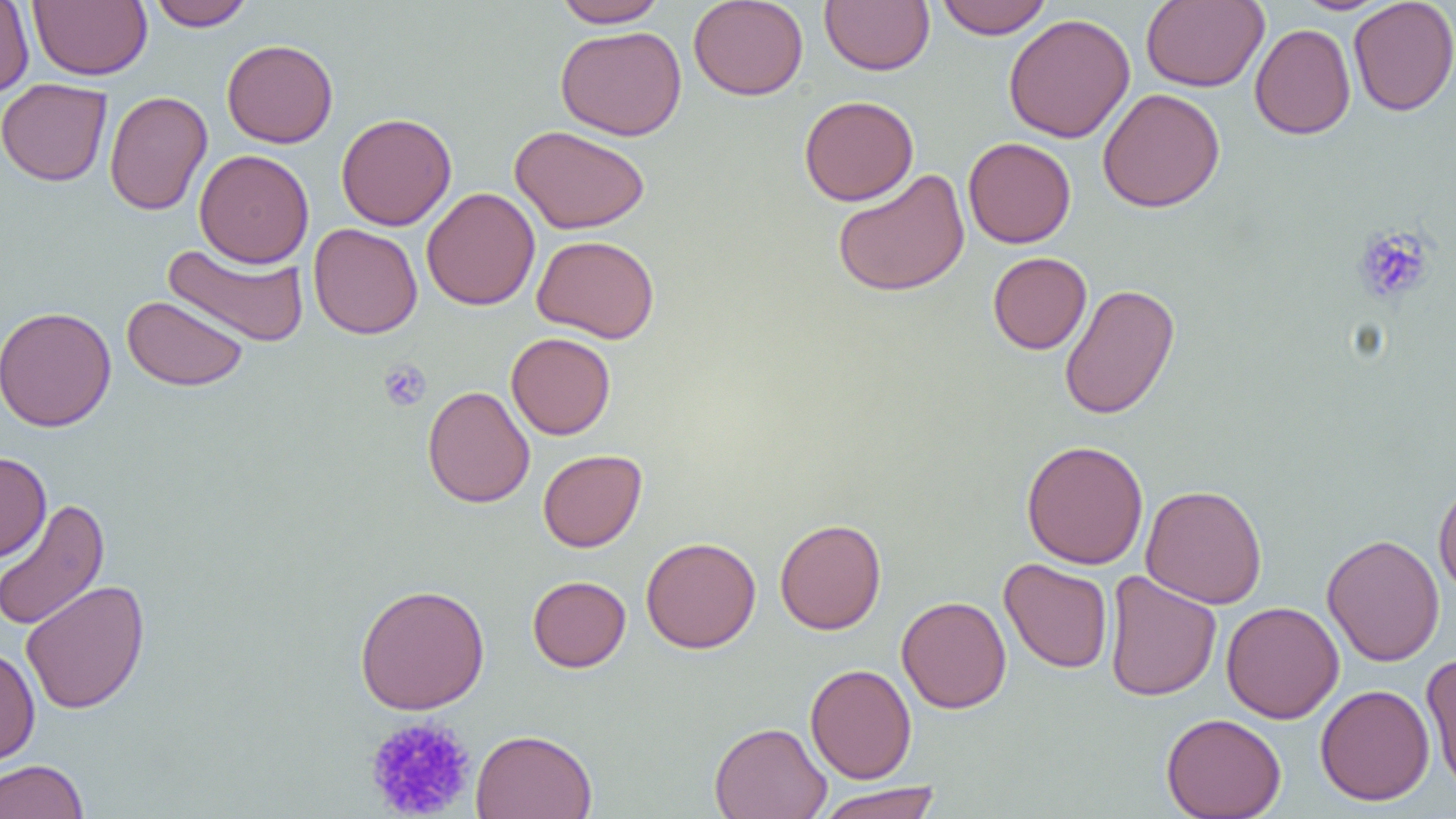
slide-level diagnosis = no evidence of blood parasites
modality = optical microscopy
uninfected red blood cell locations = approximate bounding boxes as named x1/y1/x2/y2 corners in pixels: (x1=0, y1=0, x2=35, y2=99), (x1=28, y1=0, x2=152, y2=81), (x1=146, y1=0, x2=255, y2=31), (x1=551, y1=0, x2=670, y2=28), (x1=688, y1=0, x2=809, y2=101), (x1=819, y1=0, x2=935, y2=75), (x1=935, y1=0, x2=1053, y2=39), (x1=1141, y1=0, x2=1269, y2=91), (x1=1290, y1=0, x2=1396, y2=15), (x1=1348, y1=0, x2=1456, y2=116), (x1=1003, y1=13, x2=1135, y2=143), (x1=1250, y1=23, x2=1356, y2=139), (x1=555, y1=25, x2=686, y2=140), (x1=222, y1=39, x2=339, y2=148), (x1=0, y1=78, x2=112, y2=186), (x1=1097, y1=88, x2=1225, y2=213), (x1=104, y1=90, x2=212, y2=216), (x1=798, y1=95, x2=918, y2=206), (x1=336, y1=112, x2=457, y2=231), (x1=510, y1=124, x2=650, y2=234), (x1=963, y1=137, x2=1076, y2=248), (x1=195, y1=149, x2=314, y2=268), (x1=832, y1=168, x2=970, y2=297), (x1=422, y1=187, x2=540, y2=311), (x1=308, y1=223, x2=423, y2=339), (x1=532, y1=235, x2=660, y2=343), (x1=163, y1=242, x2=309, y2=348), (x1=987, y1=252, x2=1092, y2=355), (x1=1059, y1=283, x2=1180, y2=420), (x1=121, y1=295, x2=249, y2=391), (x1=0, y1=305, x2=116, y2=432), (x1=506, y1=332, x2=616, y2=440), (x1=422, y1=385, x2=535, y2=508), (x1=1021, y1=440, x2=1149, y2=569), (x1=537, y1=449, x2=647, y2=552), (x1=0, y1=451, x2=51, y2=561), (x1=1433, y1=479, x2=1456, y2=597), (x1=1141, y1=484, x2=1268, y2=609), (x1=0, y1=498, x2=110, y2=632), (x1=774, y1=518, x2=886, y2=635), (x1=1322, y1=534, x2=1445, y2=666), (x1=641, y1=536, x2=761, y2=653), (x1=999, y1=558, x2=1113, y2=673), (x1=1103, y1=570, x2=1221, y2=702), (x1=527, y1=575, x2=631, y2=672), (x1=21, y1=580, x2=150, y2=714), (x1=354, y1=583, x2=490, y2=714), (x1=896, y1=595, x2=1012, y2=714), (x1=1221, y1=601, x2=1344, y2=724), (x1=0, y1=646, x2=40, y2=766), (x1=1421, y1=651, x2=1456, y2=797), (x1=805, y1=663, x2=917, y2=784), (x1=1315, y1=684, x2=1435, y2=806), (x1=1161, y1=713, x2=1287, y2=818), (x1=709, y1=721, x2=832, y2=819), (x1=471, y1=728, x2=598, y2=819), (x1=0, y1=759, x2=89, y2=819), (x1=814, y1=783, x2=944, y2=819)
image size = 1456×819 pixels
magnification = 1000x
field of view = one of a larger specimen
platelet locations = approximate bounding boxes as named x1/y1/x2/y2 corners in pixels: (x1=1352, y1=225, x2=1436, y2=304), (x1=378, y1=359, x2=432, y2=412), (x1=364, y1=715, x2=476, y2=818)
preparation = thin blood film